Identify the preparation type.
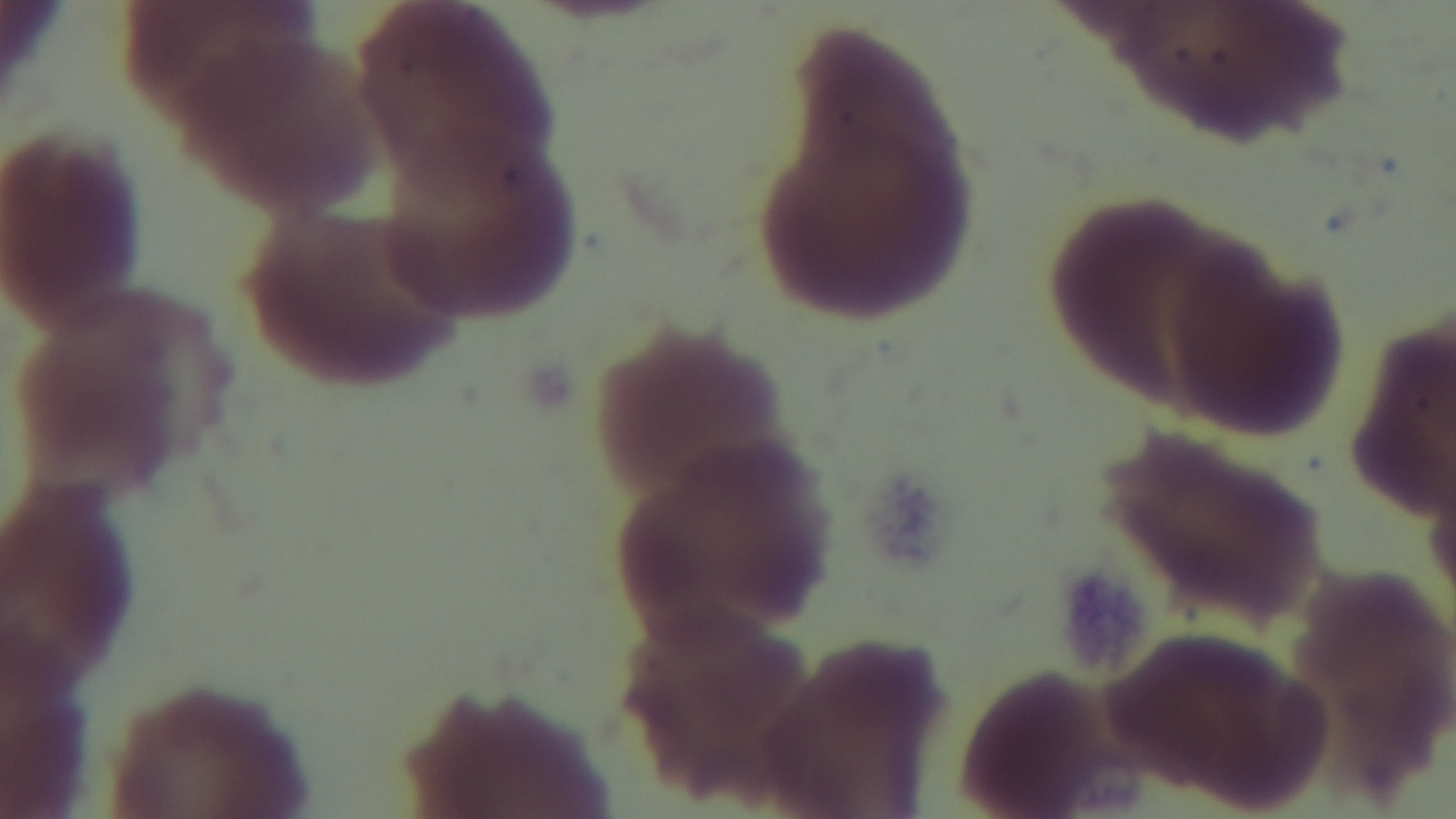

A thin smear.

malaria status = uninfected
objective = 100x oil immersion
modality = light microscopy
stain = Giemsa
capture = mounted 4K digital camera
field of view = one from the slide